Assess this cell for malaria.
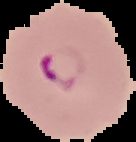
It is parasitized.

Summary:
  - Preparation: thin blood film
  - Image size: 136×142 pixels
  - Image type: segmented cell region on a black background